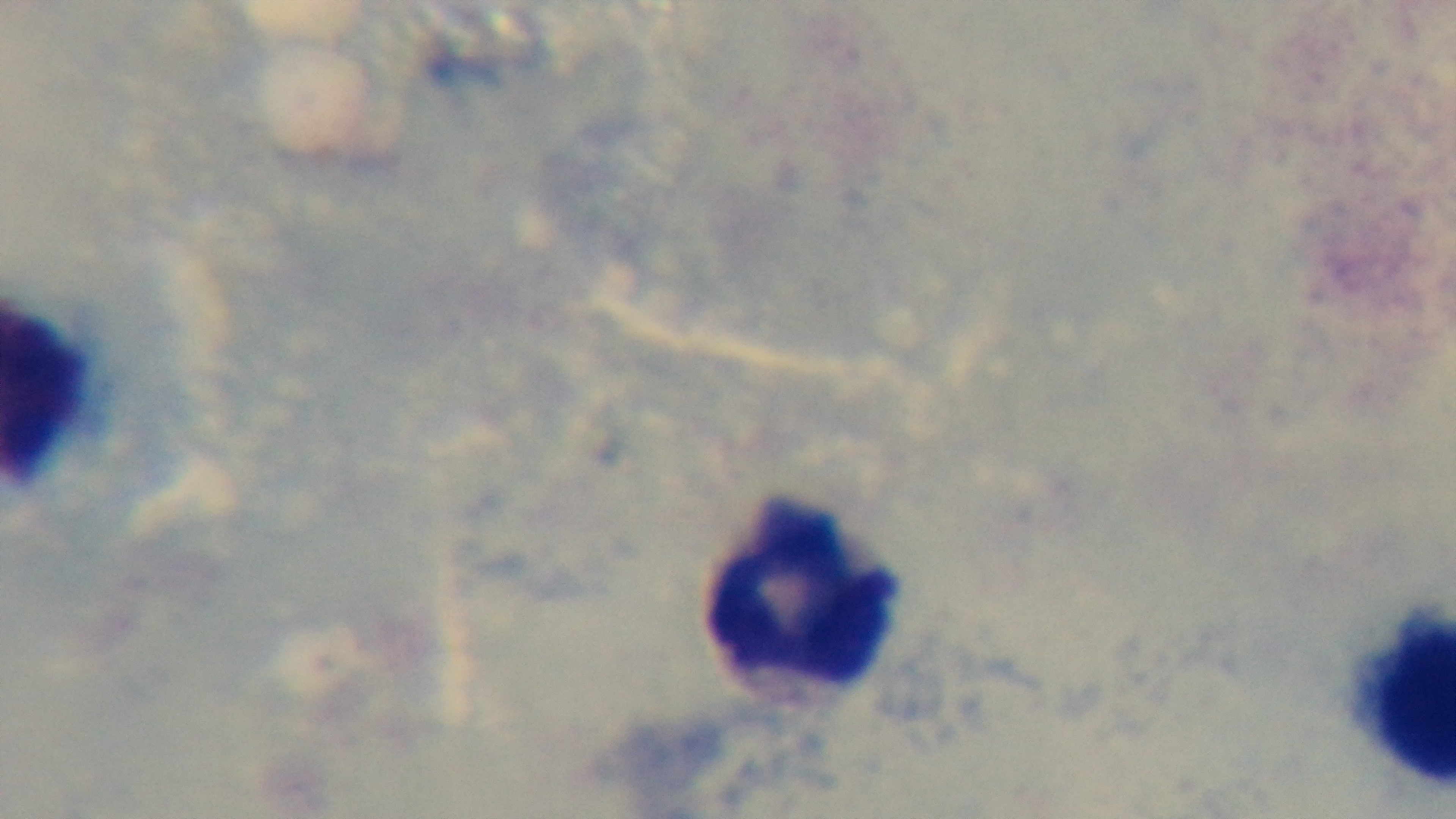 Malaria status: negative. Oil-immersion objective, 100x. Mounted 4K digital camera. Preparation: thick. Giemsa stain. One field from the slide. Light microscopy.